Outline each Babesia divergens-infected red blood cell.
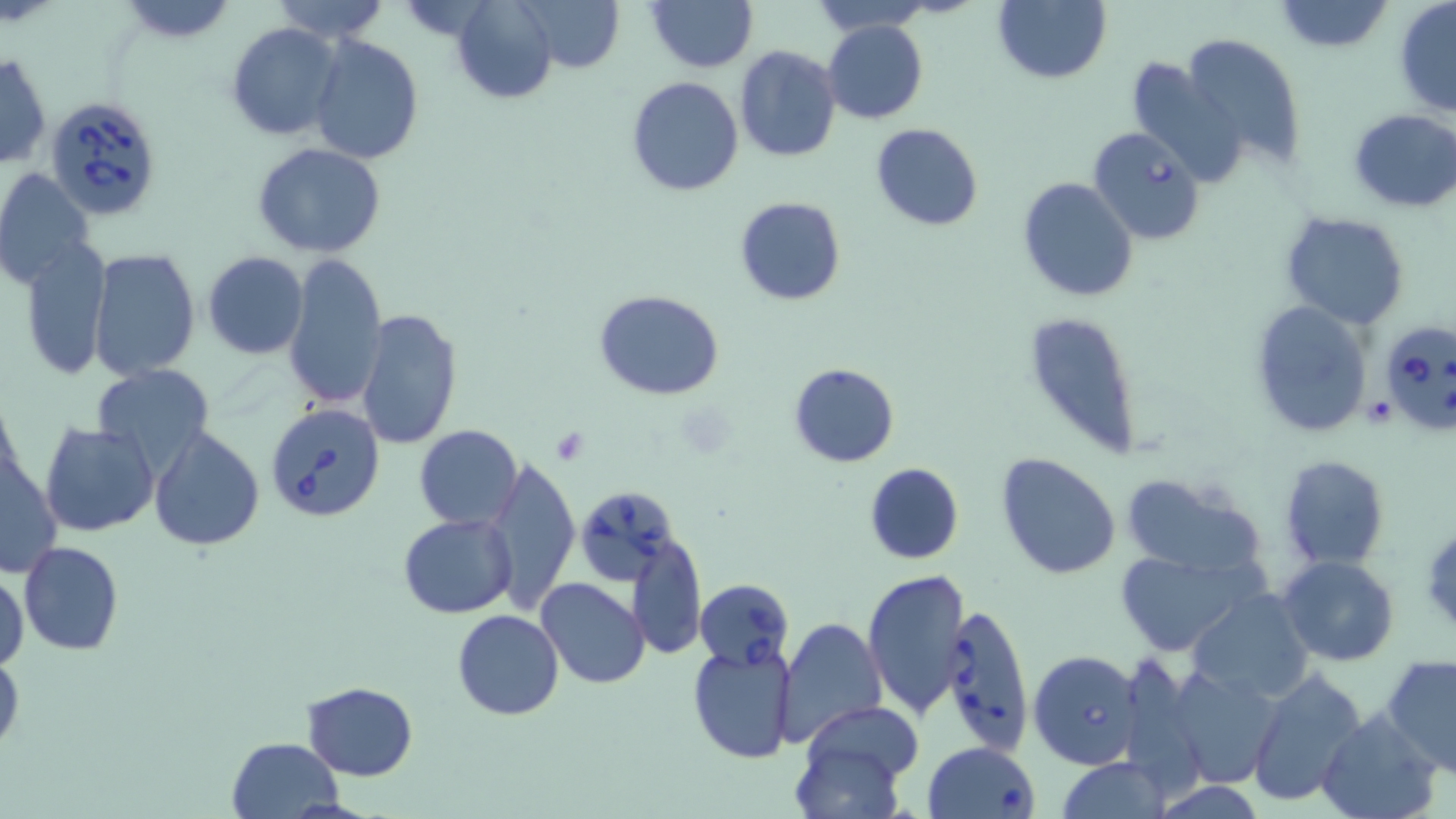
Approximate bounding boxes as (x1,y1)-(x2,y2) corner pairs in pixels.
Babesia divergens-infected red blood cells: (45,96)-(166,221), (1087,127)-(1206,245), (1377,319)-(1456,436), (264,401)-(386,524), (573,486)-(679,583), (696,578)-(795,670), (941,603)-(1034,757), (1028,649)-(1143,769), (922,741)-(1041,819).

Platelet locations: (548,428)-(592,464). Uninfected red blood cell locations: (269,0)-(390,43), (448,0)-(559,104), (514,0)-(625,72), (993,0)-(1110,85), (114,1)-(238,42), (646,1)-(757,73), (809,1)-(935,34), (1273,1)-(1393,54), (1393,2)-(1456,119), (823,19)-(928,124), (226,21)-(344,142), (1181,32)-(1306,171), (309,34)-(424,165), (733,45)-(841,164), (0,50)-(52,170), (1125,53)-(1247,191), (627,76)-(744,196), (1348,108)-(1456,213), (870,123)-(983,232), (251,143)-(386,258), (0,167)-(94,292), (1018,176)-(1139,303), (734,196)-(846,306), (1279,212)-(1409,330), (20,241)-(111,379), (87,247)-(199,380), (204,252)-(308,359), (283,252)-(387,410), (595,289)-(725,400), (1249,299)-(1373,439), (1020,310)-(1140,455), (357,311)-(462,450), (789,362)-(899,468), (93,364)-(216,477), (41,422)-(159,536), (414,424)-(521,529), (149,427)-(265,551), (994,451)-(1122,581), (1,454)-(60,578), (1279,455)-(1391,570), (484,456)-(579,610), (864,462)-(963,565), (1115,473)-(1267,580), (399,513)-(519,619), (628,531)-(707,661), (19,541)-(124,655), (1113,550)-(1258,657), (1279,555)-(1399,667), (862,567)-(970,718), (1,572)-(28,673), (535,577)-(651,690), (1187,590)-(1314,701), (454,609)-(565,720), (776,615)-(888,748), (688,641)-(795,764), (0,647)-(23,758), (1382,654)-(1456,776), (1164,665)-(1284,788), (1245,668)-(1367,807), (301,682)-(417,781), (798,703)-(921,802), (1315,709)-(1442,819), (226,738)-(344,819), (1056,757)-(1170,819), (1150,781)-(1269,818). Slide-level diagnosis: Babesia divergens. May-Grünwald-Giemsa-stained preparation. Single field of view. Thin blood smear. Light microscopy. Image is 1456×819 pixels. 1000x magnification.